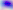
Summary:
  - Magnification: 400x
  - Identification: Toxoplasma gondii
  - Modality: micrograph